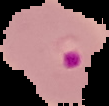

Segmented cell region on a black background. From a thin blood film. Malaria status: parasitized. Image is 109×106 pixels.